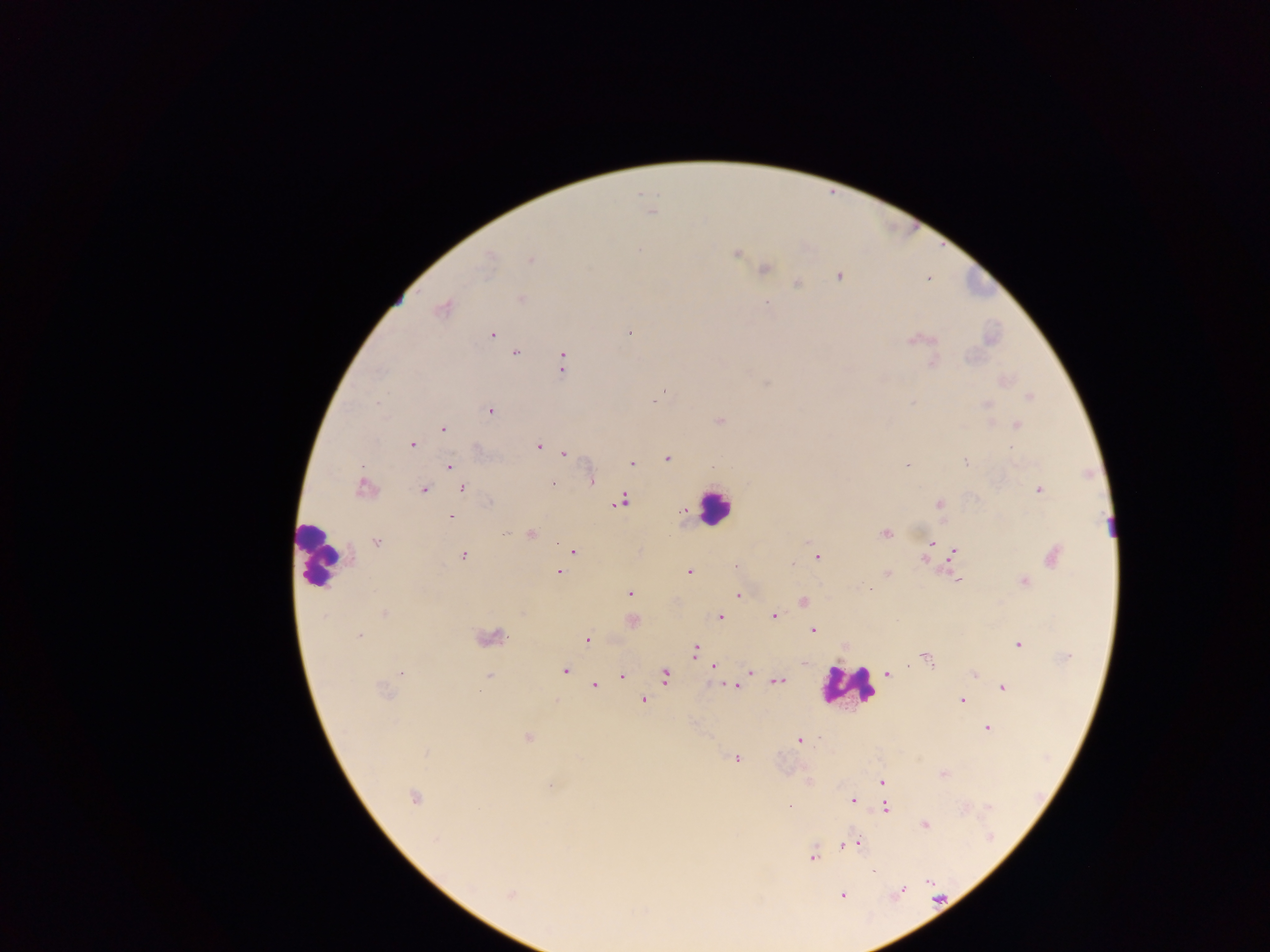

leukocyte locations = approximate centers as [x, y] in pixels: [714, 506], [318, 554], [848, 685]
capture = mobile-phone photograph through a microscope
preparation = thick blood film
field of view = single
image size = 1270×952 pixels
malaria parasite locations = approximate centers as [x, y] in pixels: [652, 212], [736, 253], [531, 259], [488, 262], [765, 269], [838, 276], [797, 284], [520, 299], [766, 303], [443, 309], [629, 333], [492, 334], [914, 340], [515, 354], [562, 363], [932, 363], [1029, 396], [654, 402], [378, 403], [986, 405], [490, 411], [720, 420], [1016, 426], [444, 429], [412, 445], [538, 446], [1011, 447], [564, 453], [668, 459], [965, 462], [631, 463], [907, 465], [449, 466], [592, 481], [553, 483], [363, 488], [462, 488], [424, 489], [1039, 490], [490, 502], [621, 502], [940, 505], [451, 516], [504, 533], [886, 533], [531, 534], [377, 542], [932, 543], [954, 551], [574, 552], [462, 556], [818, 556], [1054, 556], [925, 560], [793, 564], [736, 567], [558, 572], [689, 572], [887, 574], [955, 579], [1024, 582], [629, 593], [738, 595], [804, 602], [384, 613], [774, 616], [720, 617], [813, 630], [358, 635], [492, 637], [588, 641], [1018, 644], [695, 650], [925, 657], [1067, 658], [713, 667], [564, 671], [400, 673], [750, 673], [887, 674], [489, 675], [622, 675], [975, 675], [665, 676], [778, 681], [594, 685], [734, 686], [1003, 687], [643, 700], [961, 700], [988, 729], [527, 737], [800, 740], [426, 752], [736, 758], [943, 774], [882, 783], [550, 785], [414, 797], [852, 801], [790, 807], [886, 808], [925, 825], [849, 844], [813, 856], [872, 871], [928, 882], [901, 890], [510, 895], [842, 895]
country = Ghana